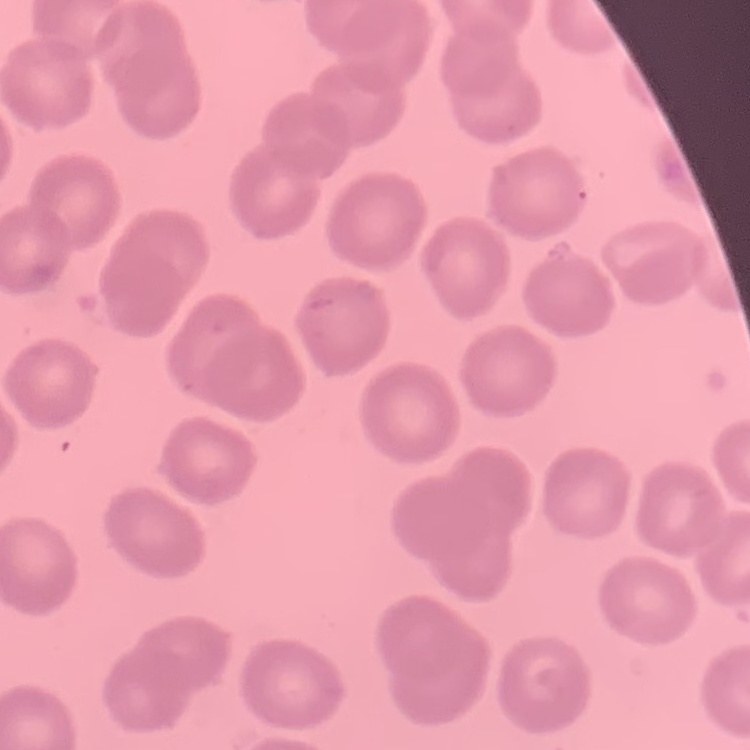
The erythrocytes exhibit no rouleaux formation. Field's or Giemsa stain. Thin blood film. Square crop of a larger photomicrograph.